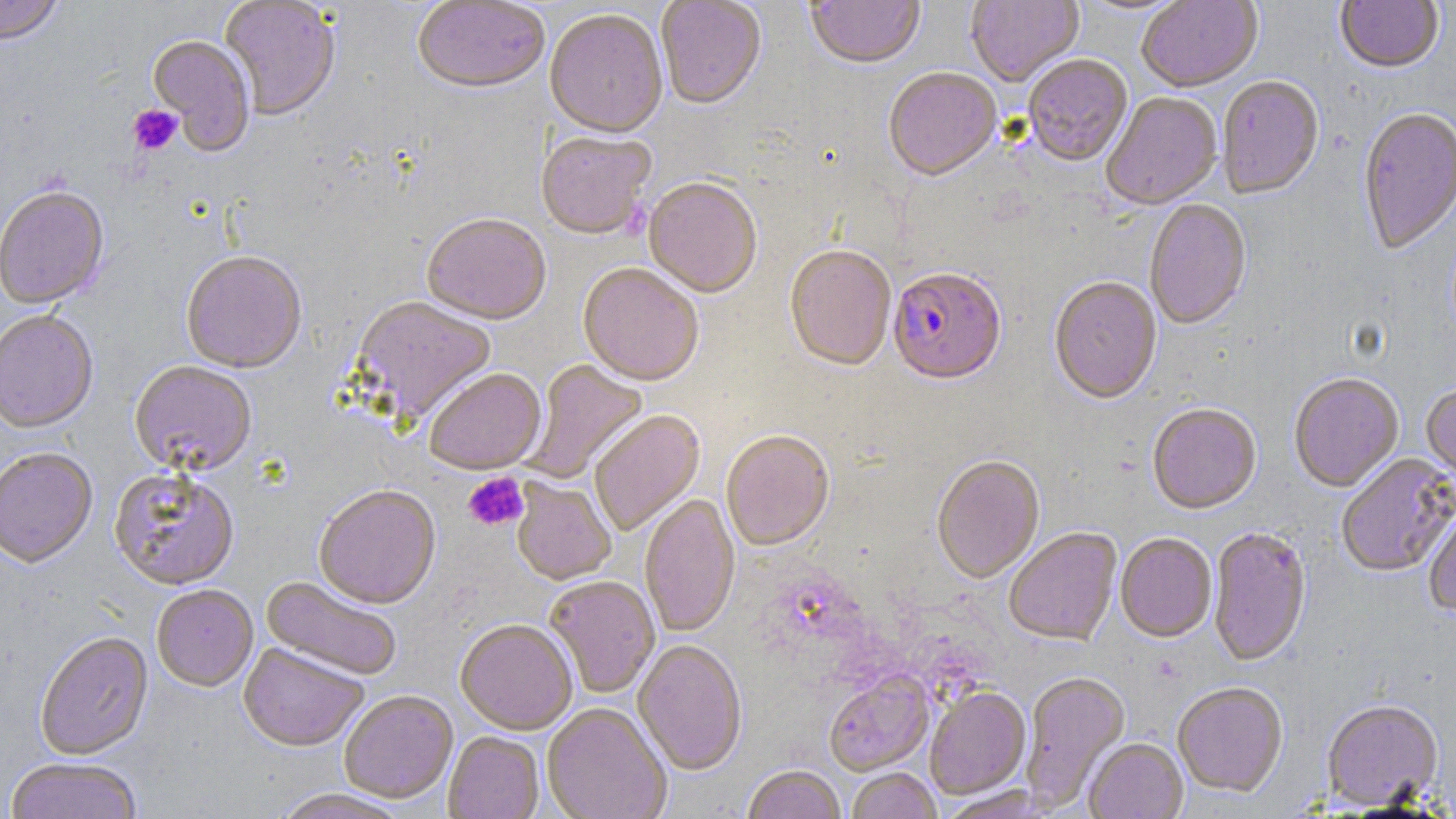
slide-level diagnosis = Plasmodium falciparum
preparation = thin blood smear
image size = 1456×819 pixels
Plasmodium falciparum-infected red blood cell locations = approximate bounding boxes as (x1,y1)-(x2,y2) corner pairs in pixels: (888,270)-(1006,388)
uninfected red blood cell locations = approximate bounding boxes as (x1,y1)-(x2,y2) corner pairs in pixels: (0,0)-(64,48), (219,0)-(341,123), (413,0)-(550,97), (656,0)-(767,112), (806,0)-(925,73), (965,0)-(1084,88), (1073,0)-(1195,17), (1336,0)-(1443,76), (1137,1)-(1263,95), (544,11)-(668,142), (148,36)-(255,156), (1023,56)-(1133,169), (883,70)-(1002,184), (1217,78)-(1325,202), (1101,94)-(1223,211), (1357,109)-(1456,257), (535,133)-(656,241), (644,180)-(762,300), (0,188)-(110,312), (1145,200)-(1252,332), (421,215)-(550,327), (785,247)-(896,373), (181,253)-(307,376), (577,265)-(703,388), (1048,279)-(1163,407), (348,297)-(497,428), (0,312)-(99,436), (521,360)-(649,483), (129,363)-(257,479), (425,371)-(547,476), (1288,375)-(1404,494), (1421,385)-(1456,484), (1147,405)-(1262,517), (589,411)-(706,537), (721,433)-(834,553), (0,450)-(98,571), (1336,454)-(1456,578), (931,457)-(1045,586), (109,470)-(240,593), (512,479)-(616,587), (314,487)-(441,611), (639,495)-(740,639), (1423,502)-(1456,621), (1208,528)-(1312,668), (1004,529)-(1122,648), (1115,534)-(1217,644), (260,577)-(401,682), (545,578)-(660,699), (152,586)-(258,693), (455,621)-(578,735), (35,634)-(155,762), (632,641)-(747,777), (238,644)-(368,753), (824,671)-(934,777), (1019,672)-(1131,811), (1172,685)-(1288,799), (925,688)-(1031,800), (339,692)-(458,805), (1321,701)-(1444,811), (542,705)-(671,819), (443,732)-(544,819), (1084,739)-(1188,819), (6,759)-(142,819), (742,767)-(846,819), (846,769)-(941,819), (938,787)-(1056,819), (268,789)-(412,819)
field of view = one of a larger specimen
modality = light microscopy
stain = May-Grünwald-Giemsa
platelet locations = approximate bounding boxes as (x1,y1)-(x2,y2) corner pairs in pixels: (127,105)-(182,156), (463,473)-(529,531)
magnification = 1000x